Report the malaria status of this cell.
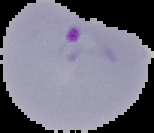
It is parasitized.

Summary:
  - Image type: cell region segmented out of the field of view; surrounding area masked to black
  - Preparation: thin blood film
  - Image size: 154×133 pixels